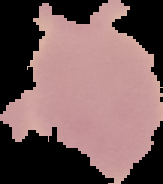

image size = 163×184 pixels
image type = cell region segmented out of the field of view; surrounding area masked to black
result = no Plasmodium parasites seen
preparation = thin blood smear